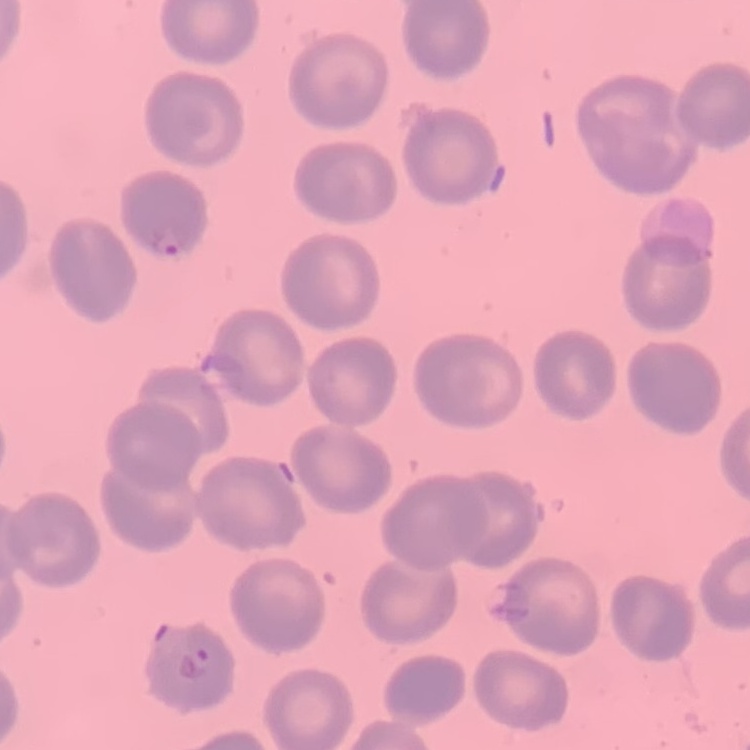

{
  "erythrocyte_morphology": "no rouleaux formation",
  "image_type": "square crop of a larger photomicrograph",
  "preparation": "thin blood film",
  "stain": "Field's or Giemsa"
}